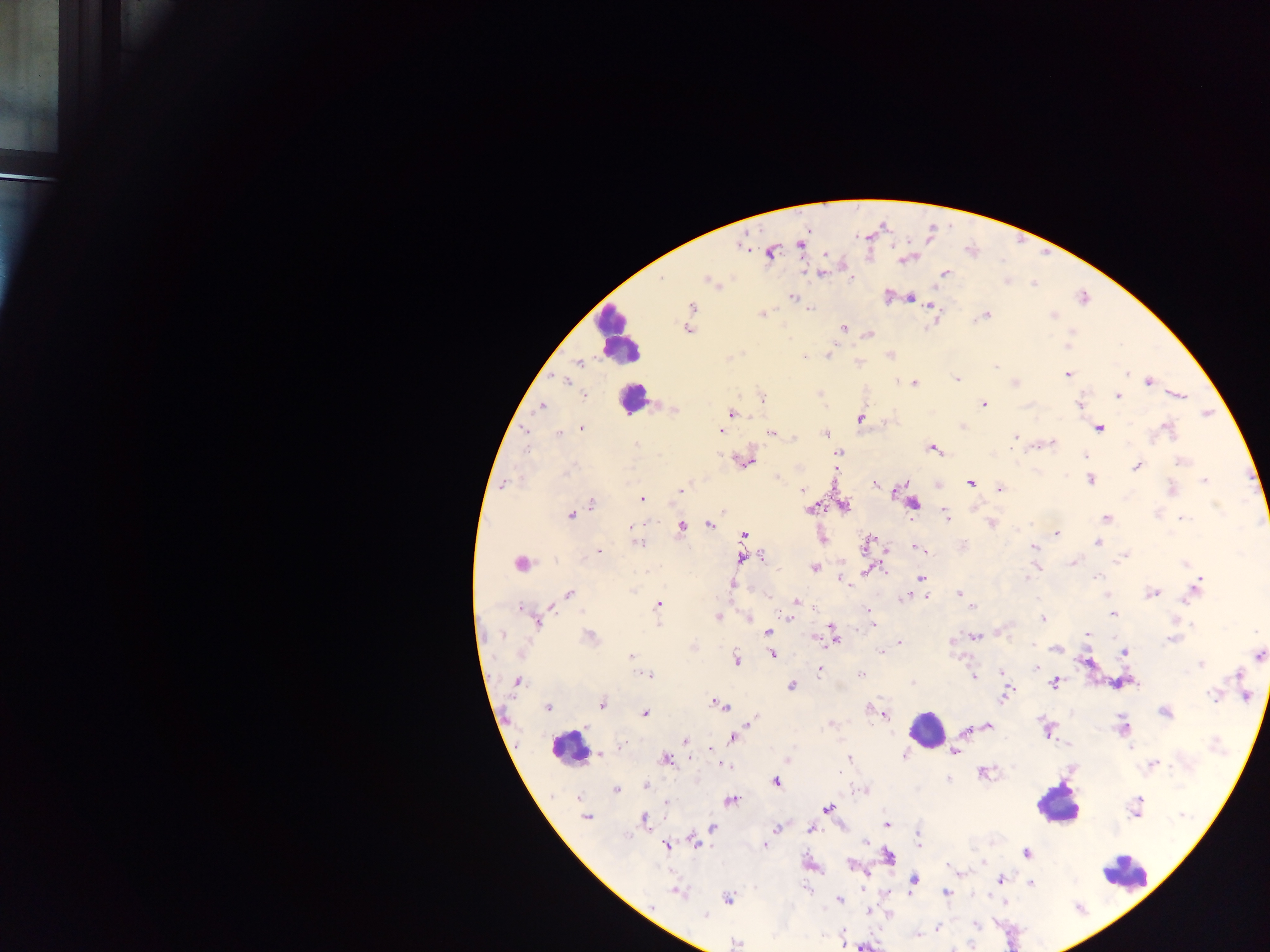

Approximate centers as (x, y) in pixels.
Summary:
  - Leukocyte locations: (618, 333), (633, 399), (927, 728), (569, 748), (1056, 804), (1127, 874)
  - Malaria parasite locations: (800, 243), (741, 246), (771, 253), (903, 259), (822, 273), (945, 273), (662, 278), (709, 281), (792, 297), (909, 298), (931, 305), (692, 307), (810, 309), (762, 314), (985, 315), (1052, 316), (843, 327), (686, 329), (1072, 331), (870, 334), (1068, 346), (829, 354), (891, 355), (804, 357), (579, 364), (995, 366), (1127, 373), (1067, 374), (957, 379), (897, 380), (1149, 381), (566, 382), (915, 383), (1015, 383), (584, 395), (1179, 395), (1117, 396), (762, 397), (984, 404), (1079, 405), (541, 406), (674, 411), (732, 414), (861, 418), (1099, 428), (582, 429), (1167, 429), (720, 430), (524, 432), (825, 433), (559, 434), (772, 434), (795, 437), (1015, 437), (1051, 444), (636, 445), (933, 449), (839, 452), (1085, 456), (745, 461), (1181, 461), (1137, 466), (778, 477), (1090, 479), (1204, 481), (970, 483), (503, 484), (876, 485), (1000, 489), (1172, 489), (802, 490), (680, 491), (641, 499), (591, 503), (913, 503), (844, 507), (810, 510), (724, 511), (571, 515), (946, 515), (1106, 517), (1184, 518), (991, 523), (709, 524), (632, 526), (682, 527), (1057, 533), (744, 535), (823, 539), (637, 543), (867, 543), (1098, 543), (915, 546), (1033, 547), (918, 549), (598, 551), (1124, 556), (762, 557), (742, 559), (1073, 562), (520, 563), (1185, 563), (814, 568), (868, 571), (1027, 577), (1097, 577), (921, 578), (842, 581), (1197, 586), (959, 593), (1152, 593), (569, 594), (1193, 594), (904, 597), (926, 598), (797, 602), (658, 605), (972, 607), (520, 608), (869, 614), (1113, 614), (717, 617), (787, 617), (749, 619), (1043, 619), (538, 623), (658, 624), (874, 624), (1256, 631), (767, 632), (833, 634), (1087, 634), (502, 635), (590, 636), (976, 637), (819, 638), (1172, 639), (899, 642), (952, 642), (1034, 645), (1056, 649), (881, 651), (1124, 652), (772, 654), (1258, 655), (631, 656), (736, 660), (1201, 665), (1037, 667), (819, 670), (1002, 672), (861, 674), (648, 675), (973, 676), (1238, 676), (517, 682), (912, 683), (1054, 683), (791, 685), (1006, 695), (1244, 695), (1213, 696), (720, 704), (602, 705), (548, 707), (869, 708), (1165, 713), (645, 714), (885, 714), (753, 719), (829, 725), (987, 727), (1123, 728), (734, 738), (686, 740), (710, 749), (955, 751), (600, 755), (905, 756), (666, 759), (849, 759), (1153, 763), (723, 765), (840, 771), (983, 772), (949, 780), (776, 781), (646, 785), (616, 791), (862, 791), (577, 797), (730, 800), (1139, 800), (667, 802), (828, 809), (586, 817), (644, 819), (887, 824), (713, 827), (776, 828), (811, 830), (918, 840), (695, 842), (865, 843), (667, 845), (764, 846), (1027, 853), (888, 856), (851, 864), (914, 880), (1000, 881), (1030, 883), (806, 888), (677, 892), (947, 893), (728, 899), (840, 900), (868, 910), (705, 916), (977, 924), (938, 929), (917, 935), (735, 943)
  - Field of view: single
  - Preparation: thick blood smear
  - Image size: 1270×952 pixels
  - Country: Ghana
  - Capture: mobile-phone photograph through a microscope